Report the malaria status of this cell.
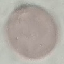
It is uninfected.

Giemsa stain. Cell patch, automatically extracted from a larger field of view and resized to 64 × 64 pixels. Photographed with a smartphone camera at the microscope eyepiece. Thin blood smear.